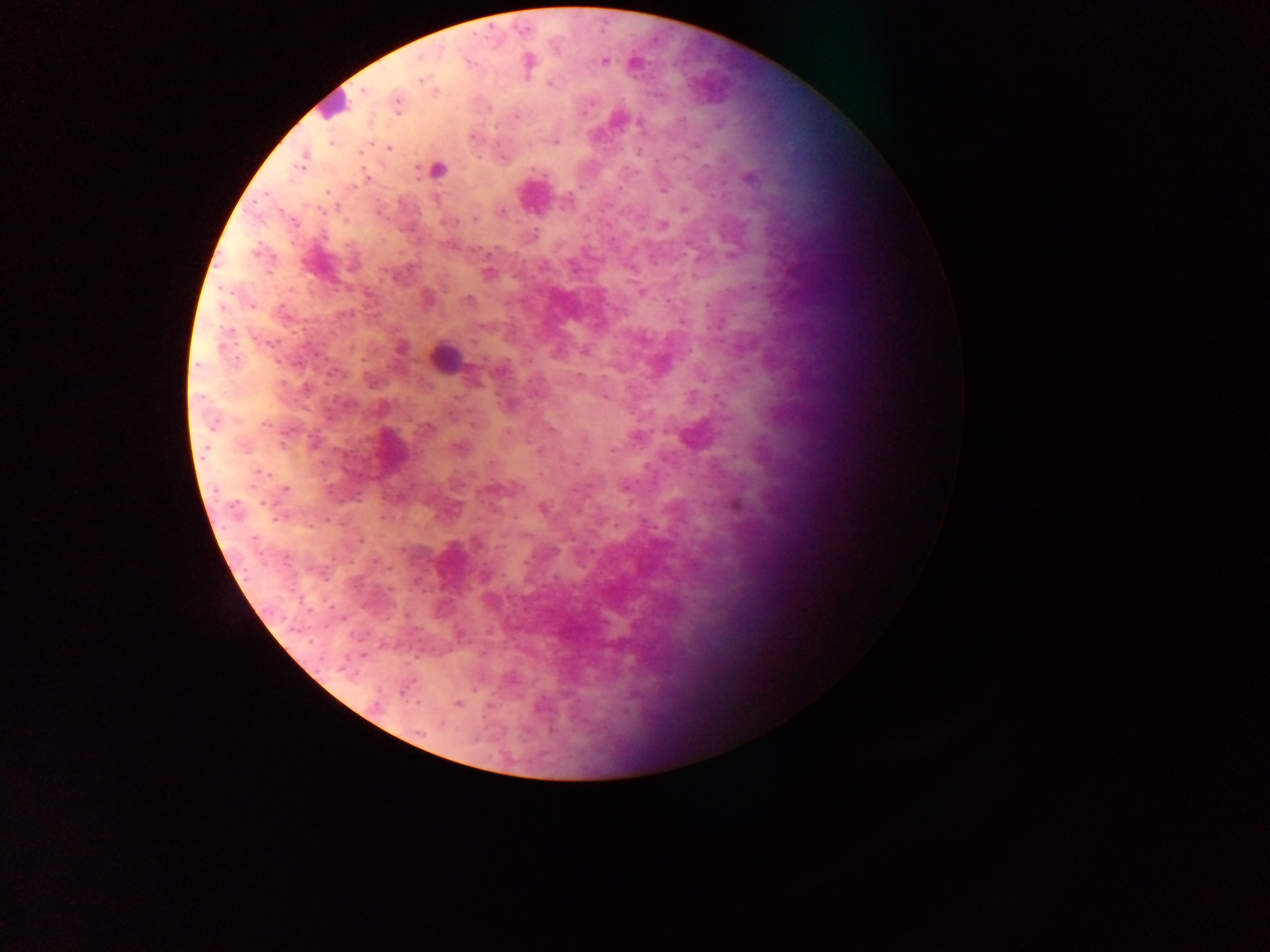
Approximate centers as [x, y] in pixels. Malaria parasite locations: [529, 61], [604, 62], [421, 79], [550, 85], [365, 90], [397, 103], [584, 112], [516, 117], [556, 142], [331, 143], [698, 145], [388, 149], [638, 152], [503, 157], [300, 166], [417, 169], [748, 178], [663, 190], [327, 191], [338, 207], [683, 209], [501, 213], [474, 220], [456, 221], [663, 225], [256, 251], [630, 268], [489, 273], [641, 292], [469, 300], [252, 306], [683, 323], [479, 325], [474, 343], [401, 348], [497, 373], [579, 375], [215, 425], [428, 427], [551, 429], [636, 439], [244, 449], [540, 451], [285, 490], [543, 507], [360, 539], [485, 575], [458, 704], [377, 705]. Leukocyte locations: [333, 105], [446, 358]. Object labeled both malaria parasite and leukocyte by the source: [438, 169]. Sample from Ghana. Thick blood smear. Mobile-phone photograph taken through the microscope. One field of view. Image is 1270×952 pixels.